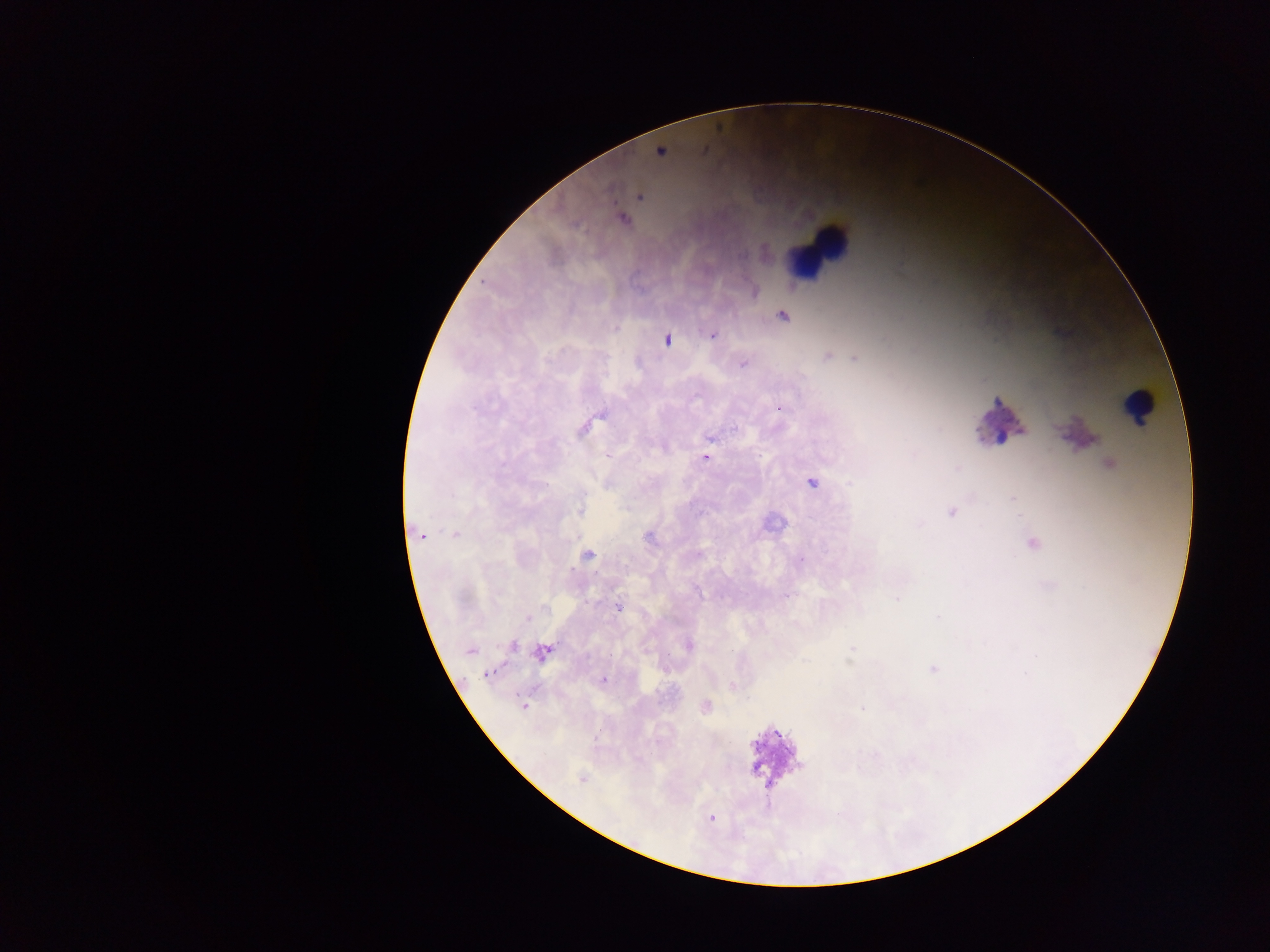 Approximate centers as [x, y] in pixels. Leukocyte locations: [815, 244], [1137, 408]. Plasmodium parasite locations: [620, 217], [783, 316], [714, 336], [827, 355], [852, 358], [744, 362], [781, 407], [915, 454], [707, 456], [957, 468], [812, 482], [420, 535], [589, 556], [802, 560], [787, 595], [618, 608], [512, 647], [471, 649], [543, 653], [606, 679], [1026, 679], [525, 706], [862, 710]. Photographed through a microscope with a mobile-phone camera. Image is 1270×952 pixels. Thick blood film. Single field of view. Collected in Ghana.